Give the extent of all Plasmodium falciparum-infected red blood cells.
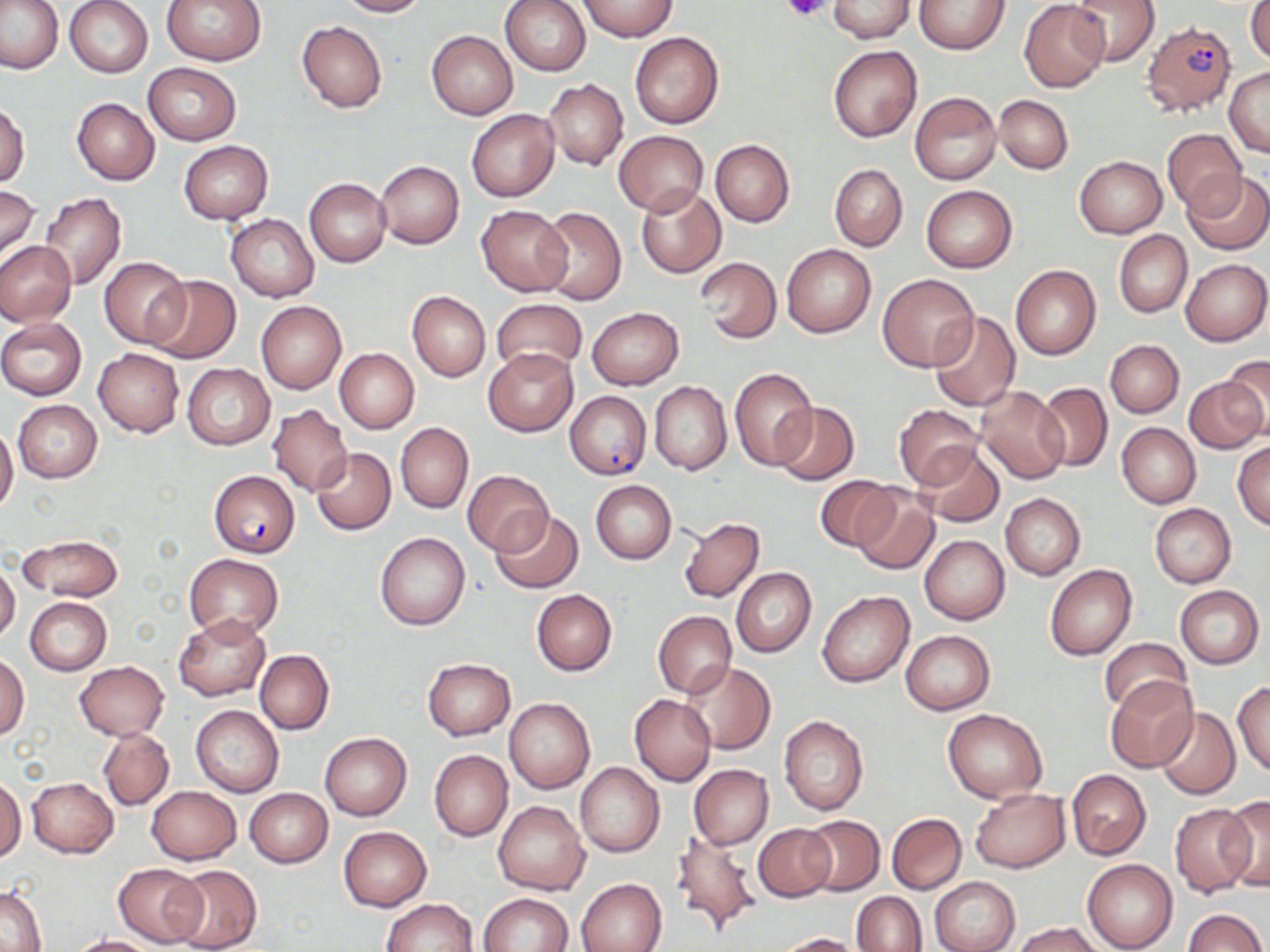

Approximate bounding boxes as (x1,y1)-(x2,y2) corner pairs in pixels.
Plasmodium falciparum-infected red blood cells: (1141,20)-(1236,117), (565,391)-(650,479), (209,470)-(300,558).

Summary:
  - Platelet locations: (783,0)-(832,23)
  - Uninfected red blood cell locations: (0,0)-(65,74), (63,0)-(154,78), (162,0)-(264,65), (336,0)-(429,17), (500,0)-(591,76), (578,0)-(677,41), (829,0)-(915,43), (1019,0)-(1110,92), (1067,0)-(1159,66), (915,1)-(1010,53), (1246,1)-(1270,65), (297,20)-(388,113), (426,30)-(518,120), (629,31)-(724,129), (828,45)-(922,143), (142,63)-(242,145), (1224,67)-(1270,157), (542,79)-(628,170), (911,91)-(1001,185), (995,94)-(1072,173), (72,98)-(159,185), (0,103)-(30,188), (466,109)-(560,202), (1163,129)-(1246,214), (614,130)-(709,216), (709,139)-(795,227), (178,140)-(273,223), (1074,156)-(1166,238), (375,161)-(464,249), (829,164)-(907,251), (1183,172)-(1270,255), (305,178)-(391,267), (921,184)-(1018,272), (0,185)-(40,264), (636,185)-(727,278), (39,193)-(125,289), (476,205)-(572,296), (536,205)-(627,304), (226,213)-(319,302), (1114,230)-(1192,317), (0,241)-(75,326), (781,243)-(876,338), (99,257)-(189,348), (696,257)-(781,344), (1181,258)-(1269,345), (1010,265)-(1101,360), (878,273)-(979,371), (145,276)-(241,364), (408,292)-(490,381), (491,297)-(587,376), (256,302)-(346,393), (587,307)-(685,389), (928,311)-(1021,411), (0,317)-(87,400), (1106,340)-(1183,417), (483,347)-(578,436), (93,348)-(184,437), (335,348)-(419,433), (1220,355)-(1270,441), (181,363)-(275,450), (731,367)-(818,469), (1184,374)-(1266,453), (649,381)-(732,475), (1034,383)-(1113,472), (976,385)-(1069,484), (13,400)-(103,482), (772,402)-(859,484), (267,404)-(352,495), (893,404)-(982,489), (395,422)-(473,513), (1117,423)-(1201,508), (0,425)-(18,515), (1233,441)-(1270,530), (915,444)-(1005,528), (311,447)-(396,535), (463,470)-(554,555), (815,476)-(901,551), (591,480)-(676,564), (850,486)-(941,576), (1000,493)-(1085,580), (1150,503)-(1236,587), (491,510)-(583,594), (677,517)-(764,603), (375,531)-(470,631), (18,535)-(123,601), (920,535)-(1009,625), (185,554)-(283,641), (0,560)-(20,644), (1044,563)-(1137,661), (732,567)-(816,658), (1174,585)-(1264,669), (532,589)-(617,675), (818,591)-(914,688), (25,596)-(111,674), (653,611)-(736,698), (173,614)-(269,700), (901,630)-(995,714), (1099,638)-(1195,718), (255,649)-(334,735), (0,654)-(29,741), (422,658)-(516,740), (73,661)-(169,740), (679,661)-(776,755), (1105,676)-(1199,773), (1232,681)-(1270,776), (629,695)-(715,786), (504,697)-(594,794), (191,705)-(283,796), (1154,707)-(1240,799), (942,709)-(1046,803), (779,715)-(869,815), (98,727)-(174,811), (320,732)-(412,820), (430,750)-(513,842), (575,761)-(665,857), (688,764)-(773,849), (1066,769)-(1150,859), (0,777)-(25,864), (27,777)-(118,858), (147,785)-(241,864), (970,787)-(1070,872), (244,788)-(332,868), (1220,796)-(1270,891), (495,801)-(588,894), (1169,805)-(1254,898), (885,812)-(966,894), (799,815)-(884,895), (754,822)-(836,901), (339,826)-(432,911), (669,830)-(763,939), (1082,859)-(1177,952), (114,862)-(205,947), (170,865)-(263,952), (930,876)-(1020,952), (576,878)-(667,952), (2,884)-(47,951), (854,888)-(1012,949), (853,891)-(927,952), (480,892)-(573,952), (379,898)-(478,952), (1182,908)-(1267,952), (1012,922)-(1104,952), (773,932)-(864,951), (72,935)-(159,952)
  - Slide-level diagnosis: Plasmodium falciparum
  - Preparation: thin blood film
  - Image size: 1270×952 pixels
  - Magnification: 1000x
  - Field of view: one of a larger specimen
  - Modality: light microscopy
  - Stain: May-Grünwald-Giemsa